Comment on the morphology of the red blood cells.
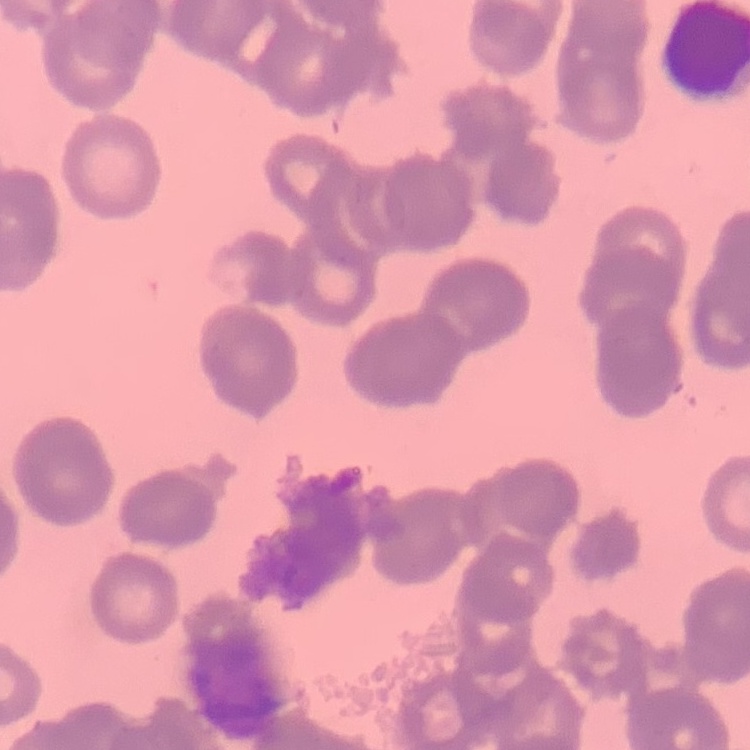
They show rouleaux formation.

One tile cut from a larger photomicrograph. Thin blood film. Field's or Giemsa stain.